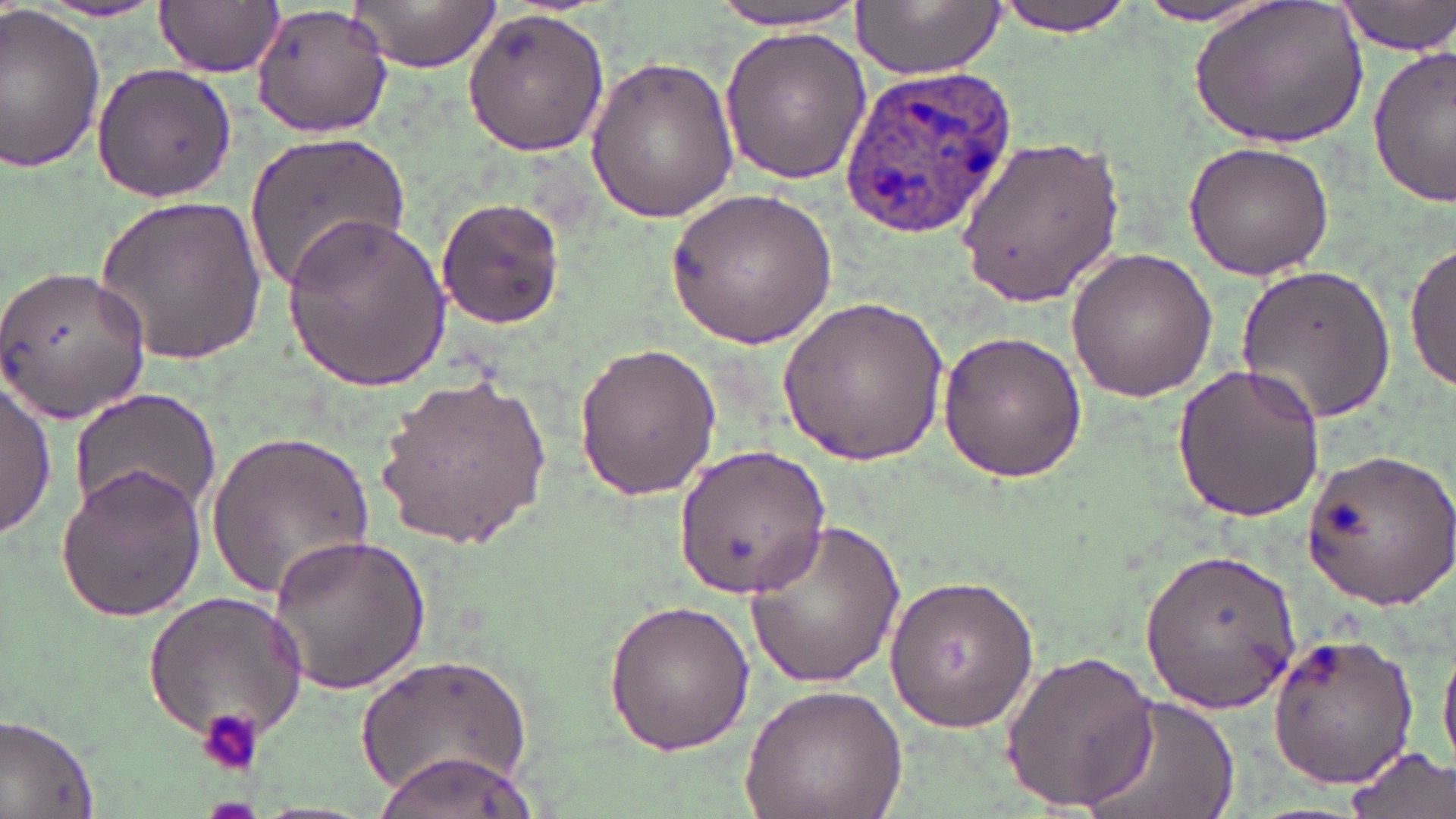

slide-level diagnosis = Plasmodium ovale
magnification = 1000x
platelet locations = approximate bounding boxes as named x1/y1/x2/y2 corners in pixels: (x1=201, y1=709, x2=263, y2=778)
modality = optical microscopy
preparation = thin blood smear
field of view = one of a larger specimen
stain = May-Grünwald-Giemsa
uninfected red blood cell locations = approximate bounding boxes as named x1/y1/x2/y2 corners in pixels: (x1=157, y1=0, x2=283, y2=79), (x1=352, y1=0, x2=498, y2=73), (x1=713, y1=0, x2=867, y2=33), (x1=854, y1=0, x2=1005, y2=78), (x1=993, y1=0, x2=1137, y2=37), (x1=1190, y1=0, x2=1371, y2=152), (x1=1337, y1=0, x2=1456, y2=57), (x1=248, y1=1, x2=396, y2=139), (x1=1125, y1=1, x2=1285, y2=28), (x1=34, y1=2, x2=170, y2=24), (x1=0, y1=7, x2=105, y2=173), (x1=461, y1=9, x2=609, y2=158), (x1=719, y1=26, x2=873, y2=184), (x1=1368, y1=47, x2=1455, y2=206), (x1=584, y1=56, x2=740, y2=223), (x1=91, y1=60, x2=237, y2=203), (x1=245, y1=131, x2=408, y2=296), (x1=958, y1=134, x2=1122, y2=307), (x1=1181, y1=140, x2=1336, y2=281), (x1=666, y1=187, x2=842, y2=350), (x1=96, y1=192, x2=267, y2=367), (x1=435, y1=197, x2=565, y2=329), (x1=277, y1=212, x2=451, y2=391), (x1=1406, y1=234, x2=1454, y2=393), (x1=1066, y1=247, x2=1218, y2=402), (x1=1234, y1=262, x2=1398, y2=424), (x1=0, y1=265, x2=156, y2=422), (x1=778, y1=293, x2=955, y2=465), (x1=935, y1=328, x2=1090, y2=482), (x1=572, y1=339, x2=722, y2=500), (x1=1172, y1=361, x2=1327, y2=522), (x1=377, y1=372, x2=554, y2=547), (x1=0, y1=377, x2=56, y2=540), (x1=66, y1=386, x2=222, y2=524), (x1=204, y1=430, x2=374, y2=603), (x1=673, y1=443, x2=832, y2=598), (x1=1300, y1=445, x2=1456, y2=611), (x1=53, y1=464, x2=208, y2=623), (x1=744, y1=518, x2=910, y2=687), (x1=267, y1=531, x2=431, y2=697), (x1=1141, y1=542, x2=1302, y2=711), (x1=883, y1=573, x2=1040, y2=735), (x1=142, y1=588, x2=309, y2=749), (x1=601, y1=597, x2=757, y2=755), (x1=1261, y1=631, x2=1420, y2=788), (x1=1439, y1=637, x2=1456, y2=776), (x1=996, y1=647, x2=1163, y2=813), (x1=358, y1=652, x2=535, y2=803), (x1=738, y1=685, x2=908, y2=819), (x1=1074, y1=692, x2=1240, y2=819), (x1=0, y1=712, x2=101, y2=819), (x1=1343, y1=746, x2=1455, y2=819), (x1=379, y1=753, x2=540, y2=819)
Plasmodium ovale-infected red blood cell locations = approximate bounding boxes as named x1/y1/x2/y2 corners in pixels: (x1=840, y1=69, x2=1019, y2=238)
image size = 1456×819 pixels